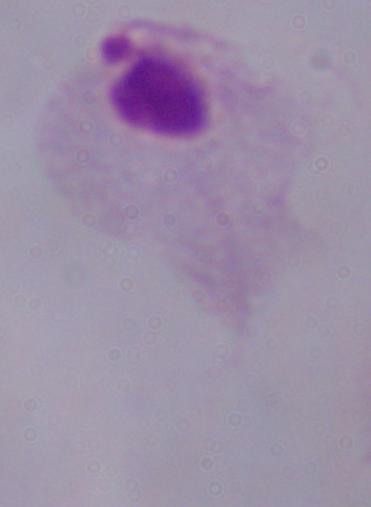 Micrograph. A trichomonad is shown. Captured at 1000x magnification.